Report the malaria status of this cell.
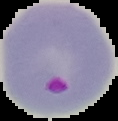

Parasitized.

Image is 118×121 pixels. From a thin blood film. Cell region segmented out of the field of view; the surrounding area is masked to black.